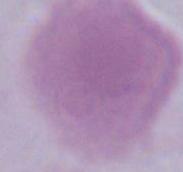 Photomicrograph. Captured at 1000x magnification. An erythrocyte is seen.